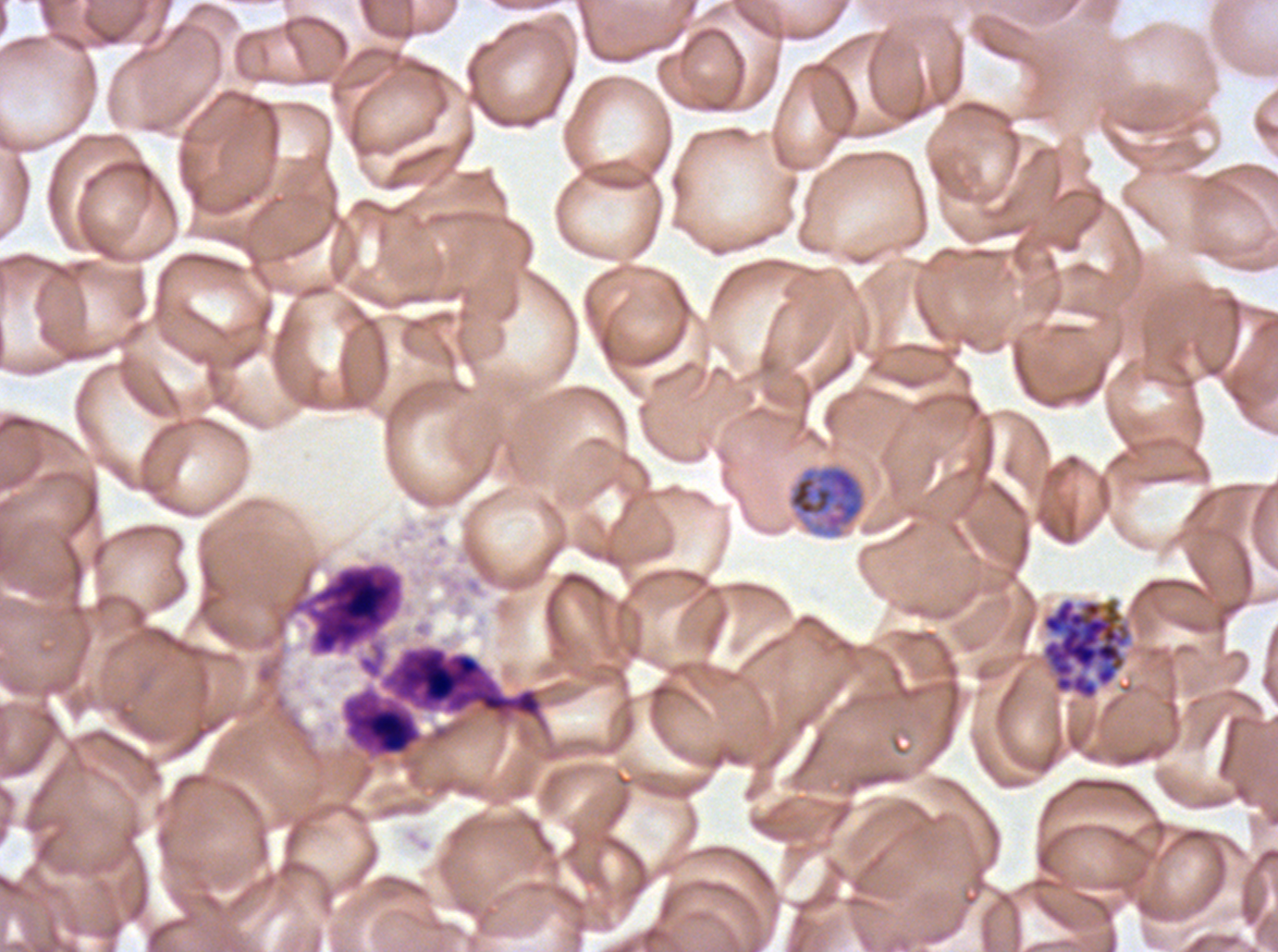

notation = approximate bounding boxes as {x1, y1, x2, y2} in pixels
segmenter locations = {1040, 596, 1133, 701}
leukocyte locations = {306, 564, 402, 654}, {341, 644, 543, 757}
early schizont locations = {787, 463, 866, 539}
preparation = thin blood smear
life-cycle stages observed = early schizont, segmenter
specimen = Plasmodium falciparum from a patient in The Gambia, cultured ex vivo for 24 to 48 hours
field of view = one sub-image of a larger composite
image size = 1278×952 pixels
stain = Giemsa